Assess this cell for malaria.
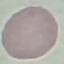
Uninfected.

Summary:
  - Image type: automatically extracted cell patch, resized to 64 × 64 pixels
  - Capture: smartphone through the microscope eyepiece
  - Stain: Giemsa
  - Preparation: thin smear